State which cell type is depicted.
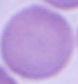

This is an erythrocyte.

Summary:
  - Magnification: 1000x
  - Modality: photomicrograph